Comment on the morphology of the red blood cells.
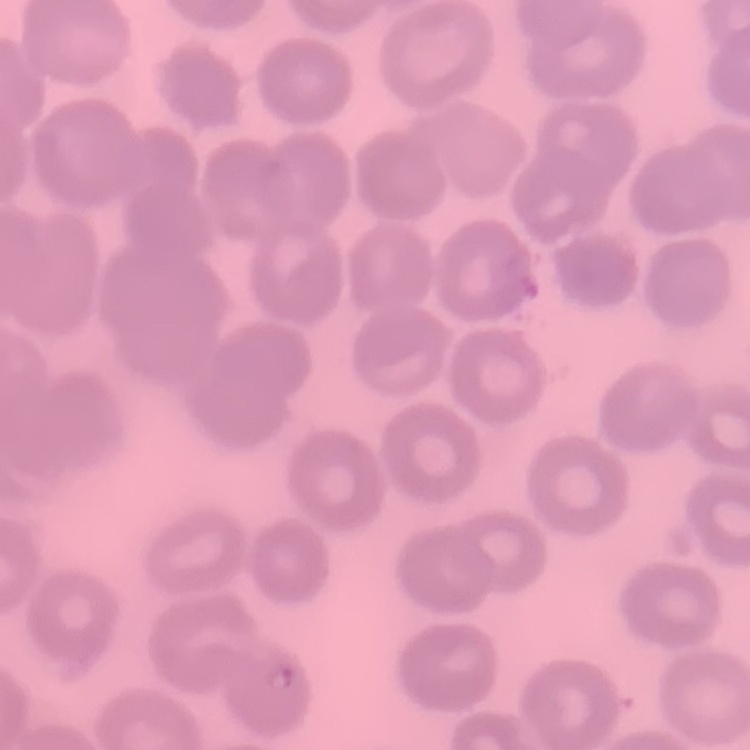
They show no rouleaux formation.

Square crop of a larger photomicrograph. Thin peripheral smear. Field's or Giemsa stain.